Identify the cell.
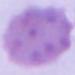

This is an erythrocyte.

modality: micrograph
magnification: 1000x